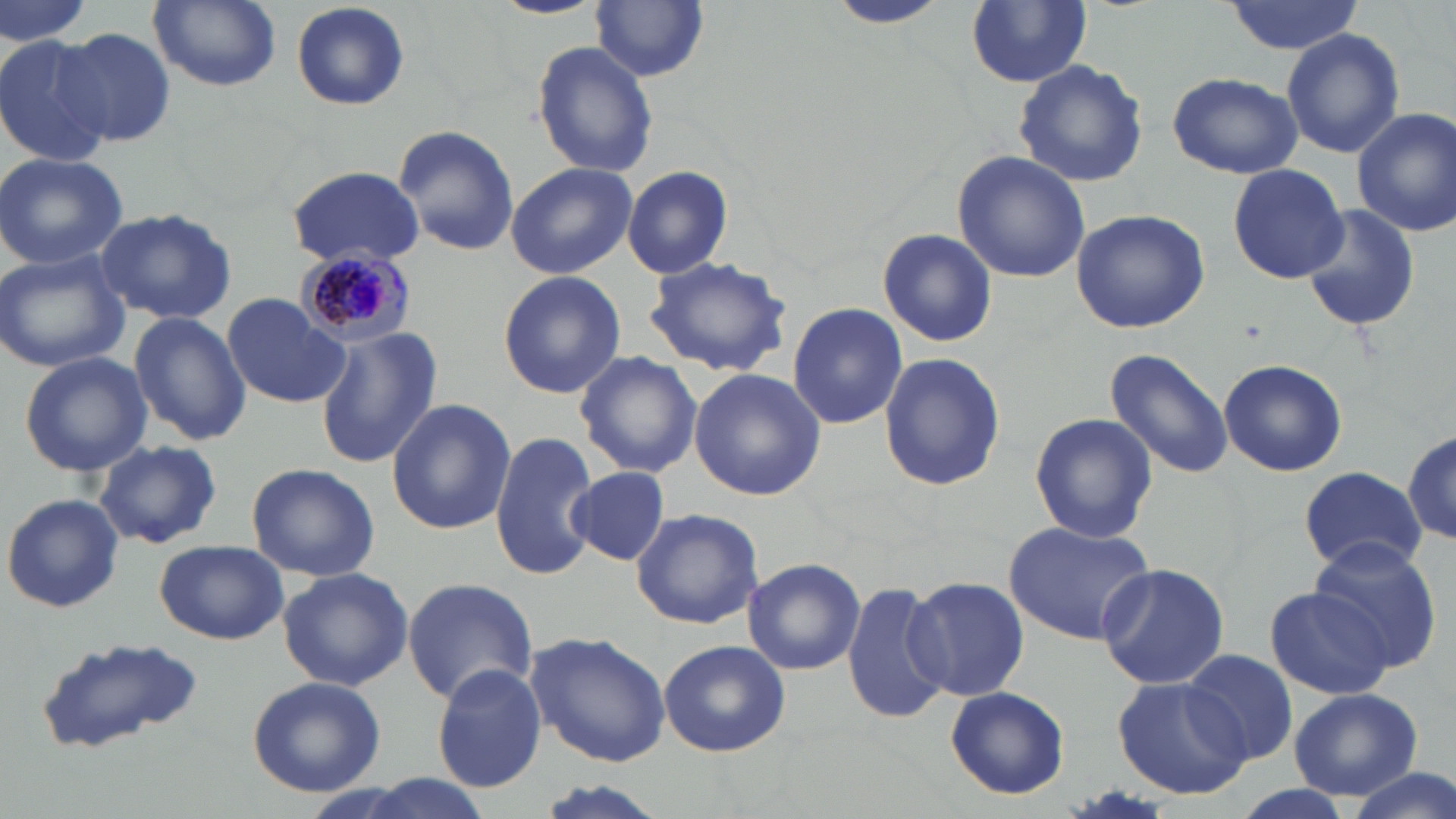
Summary:
  - Coordinate format: approximate bounding boxes as (x1,y1)-(x2,y2) corner pairs in pixels
  - Plasmodium malariae-infected red blood cell locations: (294,246)-(416,348)
  - Uninfected red blood cell locations: (0,0)-(95,52), (148,0)-(282,91), (491,0)-(605,19), (592,1)-(709,82), (827,1)-(954,30), (965,1)-(1092,87), (1221,1)-(1363,54), (292,3)-(410,112), (57,26)-(177,148), (1281,27)-(1403,157), (0,33)-(116,169), (532,41)-(659,178), (1014,59)-(1149,188), (1166,70)-(1303,179), (1353,106)-(1456,238), (395,124)-(517,256), (953,152)-(1092,284), (0,153)-(130,270), (506,162)-(637,278), (1226,162)-(1350,284), (287,164)-(426,267), (622,165)-(734,279), (1299,203)-(1421,333), (95,206)-(239,325), (1069,208)-(1210,333), (876,228)-(997,347), (0,250)-(129,374), (643,253)-(794,377), (497,271)-(626,398), (223,293)-(348,408), (788,302)-(909,429), (129,314)-(250,447), (315,328)-(441,468), (1103,349)-(1236,479), (878,351)-(1006,491), (18,352)-(152,477), (576,353)-(701,477), (1217,358)-(1348,477), (690,368)-(827,500), (387,398)-(515,535), (1028,413)-(1158,544), (1402,428)-(1456,550), (490,431)-(600,581), (94,441)-(222,548), (246,462)-(380,581), (567,466)-(672,566), (1297,466)-(1426,574), (2,493)-(124,614), (631,507)-(765,629), (1005,521)-(1154,643), (1306,538)-(1445,674), (154,540)-(290,645), (743,557)-(865,676), (1095,561)-(1229,688), (278,567)-(412,690), (908,576)-(1029,701), (402,577)-(538,703), (843,581)-(950,724), (1262,584)-(1397,701), (524,630)-(672,766), (30,639)-(209,755), (658,640)-(789,756), (1182,648)-(1302,765), (431,663)-(548,792), (1114,676)-(1252,798), (248,677)-(386,796), (1287,685)-(1424,802), (946,687)-(1069,799), (1340,767)-(1454,819)
  - Slide-level diagnosis: Plasmodium malariae
  - Preparation: thin blood smear
  - Image size: 1456×819 pixels
  - Modality: light microscopy
  - Magnification: 1000x
  - Stain: May-Grünwald-Giemsa
  - Field of view: single